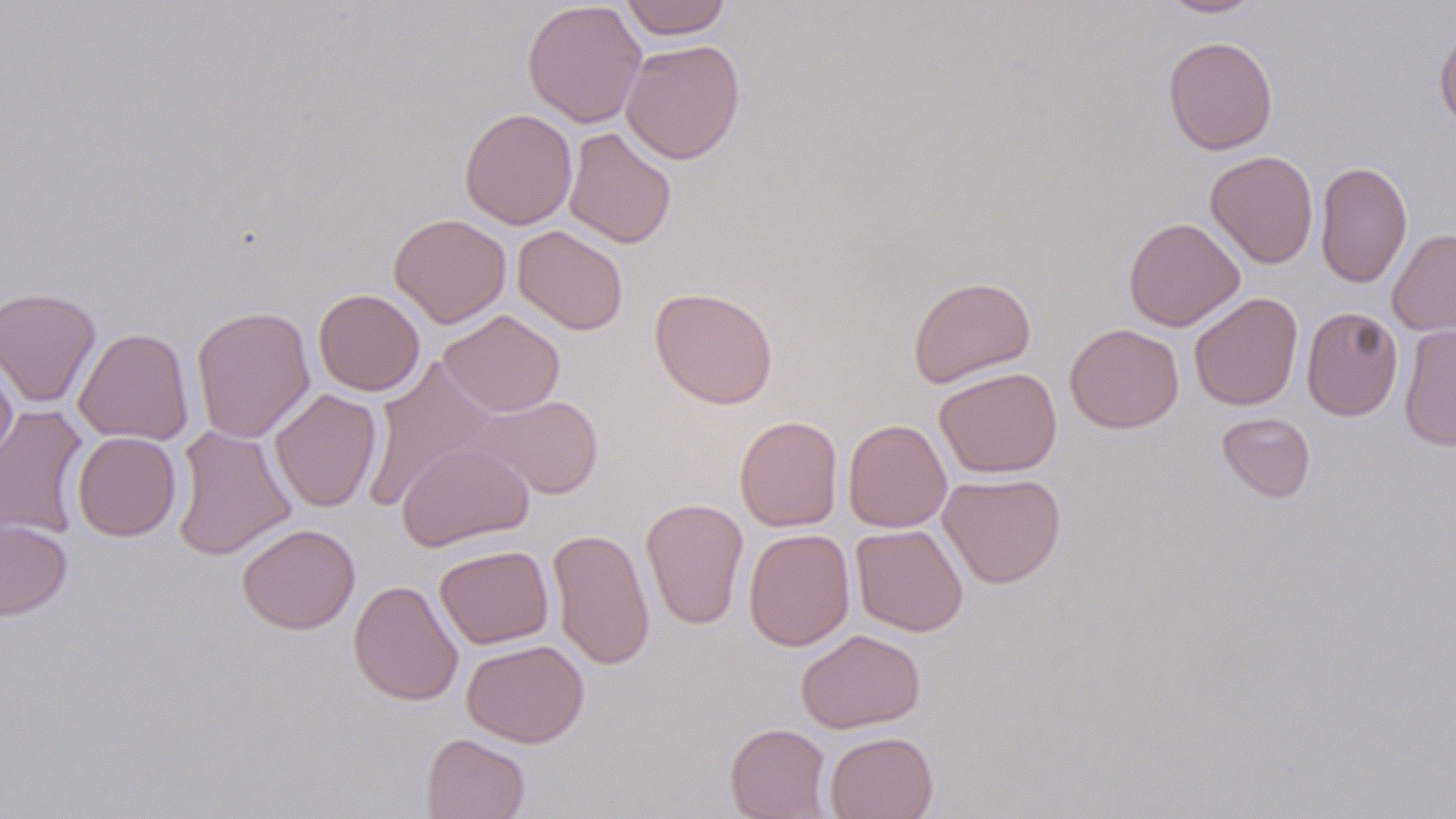
slide-level diagnosis = negative for blood parasites
preparation = thin blood smear
uninfected red blood cell locations = approximate bounding boxes as (x1,y1)-(x2,y2) corner pairs in pixels: (522,0)-(647,128), (618,0)-(732,39), (1158,0)-(1265,18), (1433,25)-(1456,130), (1163,35)-(1278,155), (620,39)-(745,164), (460,108)-(577,230), (563,126)-(677,249), (1205,150)-(1319,269), (1315,159)-(1413,288), (389,213)-(512,328), (1123,217)-(1245,331), (513,225)-(629,335), (1387,228)-(1456,337), (908,275)-(1036,388), (0,286)-(101,408), (650,286)-(779,409), (313,288)-(425,396), (1189,292)-(1303,410), (191,305)-(316,444), (1301,306)-(1403,421), (438,310)-(565,417), (1065,323)-(1184,434), (1398,323)-(1456,451), (74,327)-(194,445), (0,355)-(17,471), (362,358)-(497,511), (934,366)-(1062,478), (269,388)-(382,512), (469,394)-(604,499), (0,405)-(89,541), (1217,412)-(1315,502), (734,415)-(843,532), (843,418)-(952,532), (171,424)-(296,561), (72,432)-(181,541), (397,440)-(535,551), (938,472)-(1066,589), (641,498)-(749,630), (0,519)-(71,620), (237,523)-(360,634), (850,524)-(968,637), (548,527)-(656,670), (743,529)-(855,651), (435,545)-(554,649), (349,579)-(463,706), (796,629)-(925,734), (461,639)-(589,747), (725,723)-(832,819), (824,731)-(939,819), (421,733)-(530,819)
magnification = 1000x
image size = 1456×819 pixels
field of view = single
modality = optical microscopy
stain = May-Grünwald-Giemsa